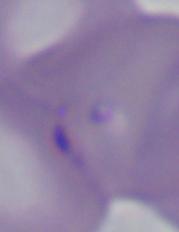
modality = photomicrograph
identification = Babesia
magnification = 1000x